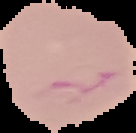
{
  "image_type": "segmented cell region with the area outside set to black",
  "preparation": "thin blood smear",
  "result": "malaria parasites identified",
  "image_size": "136×133 pixels"
}